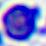
magnification: 400x
modality: photomicrograph
identification: white blood cell